Give the position of every leukocyte visible.
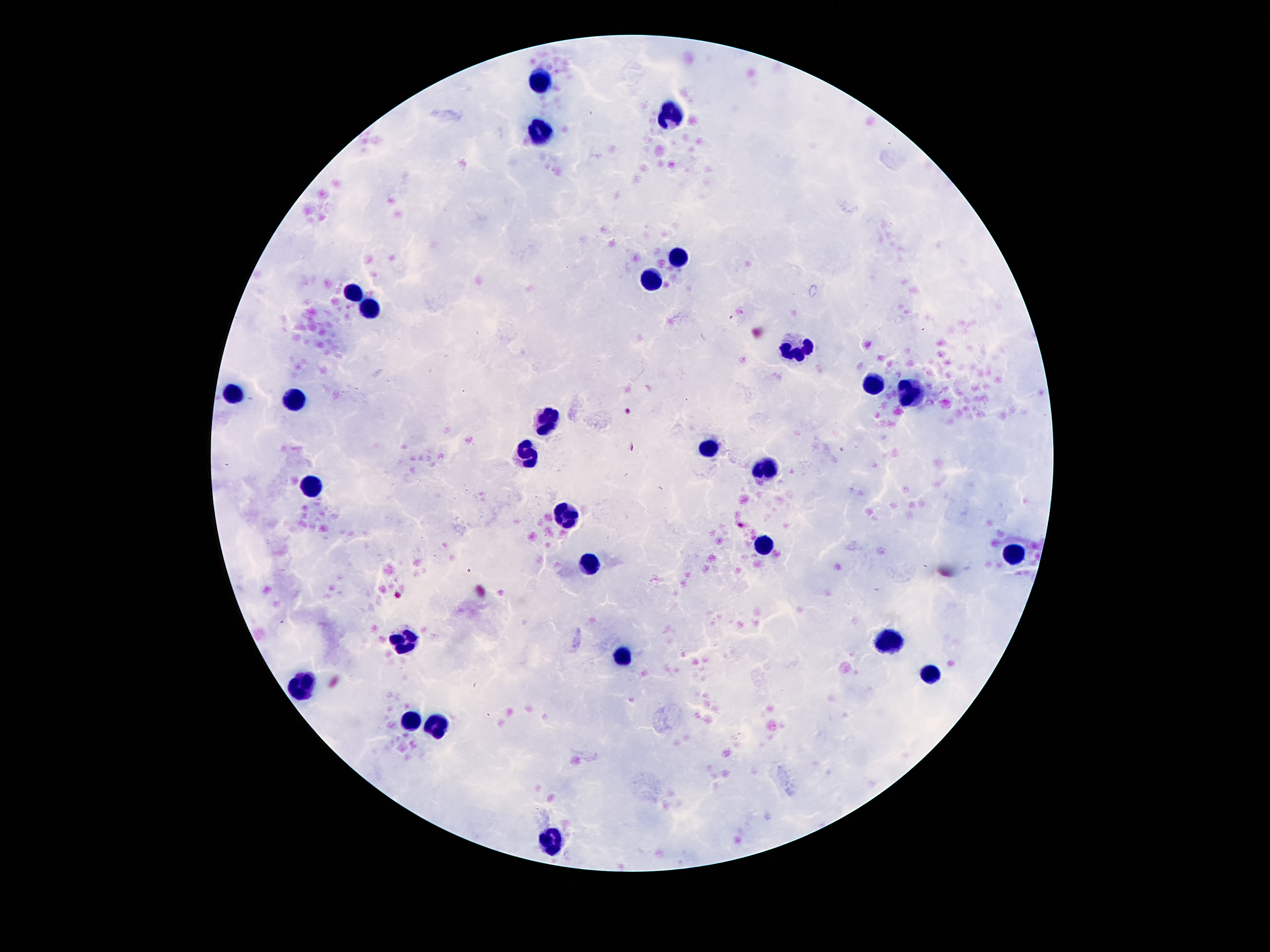
Approximate centers as {x, y} in pixels.
Leukocytes: {539, 83}, {667, 114}, {539, 134}, {678, 251}, {654, 282}, {353, 295}, {369, 308}, {797, 348}, {872, 383}, {912, 392}, {232, 394}, {295, 401}, {548, 421}, {709, 446}, {528, 454}, {767, 468}, {313, 484}, {565, 516}, {762, 547}, {1016, 554}, {590, 563}, {890, 640}, {404, 642}, {621, 658}, {932, 674}, {304, 684}, {410, 722}, {441, 726}, {552, 840}.

Single field of view. 100x magnification. Photographed through the microscope eyepiece with a smartphone camera. Giemsa-stained preparation. Image is 1270×952 pixels. Patient malaria status: uninfected. Thick blood film.